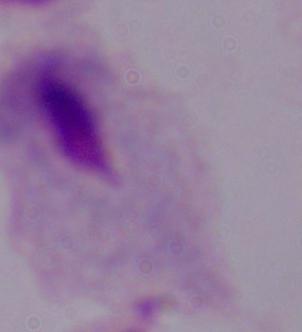

Summary:
  - Magnification: 1000x
  - Modality: photomicrograph
  - Identification: trichomonad